Locate every malaria parasite.
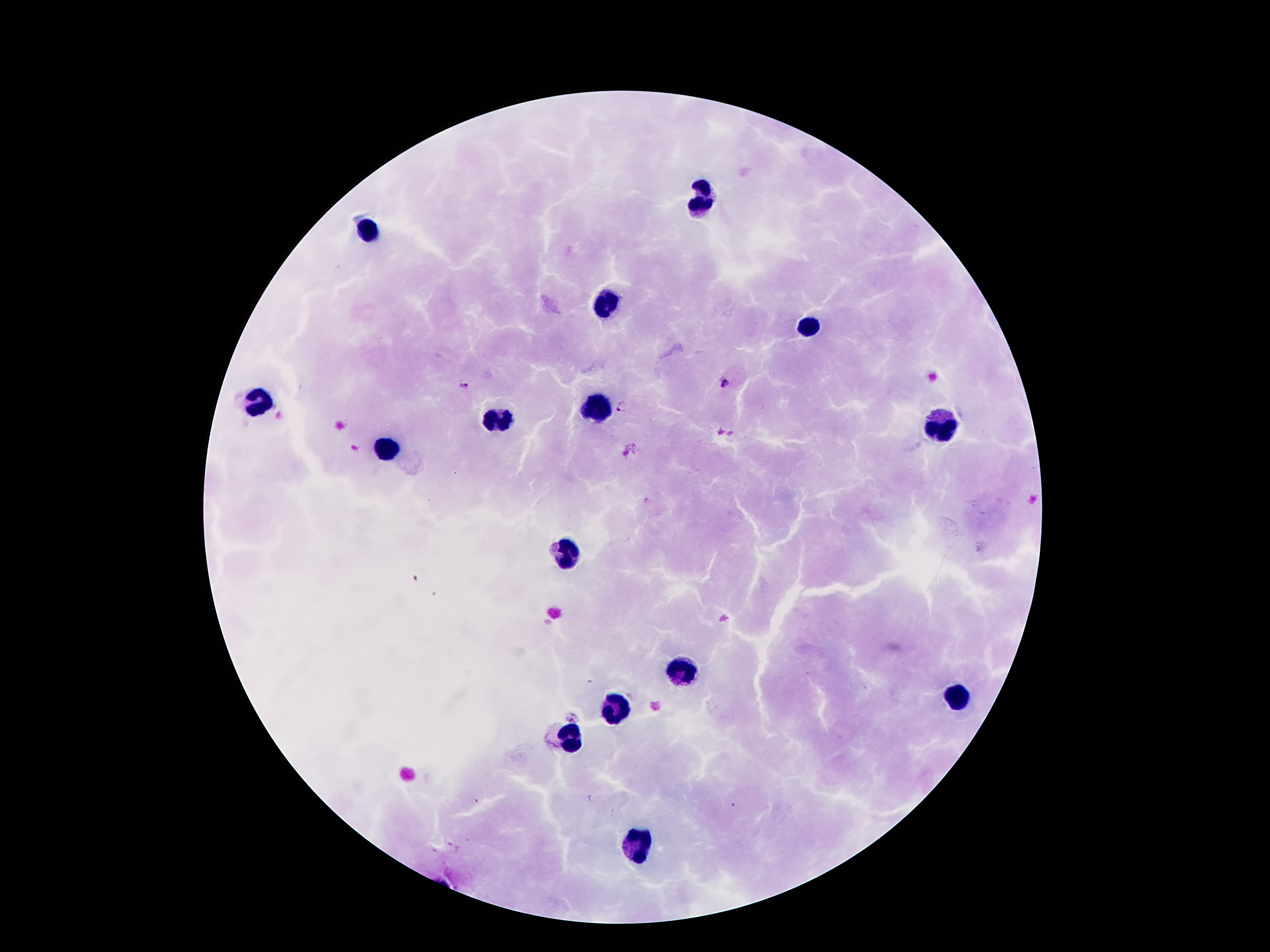

Approximate centers as (x, y) in pixels.
Malaria parasites: (464, 384), (725, 384), (622, 406).

Summary:
  - Leukocyte locations: (703, 195), (369, 231), (608, 300), (808, 324), (256, 403), (599, 406), (498, 419), (942, 425), (384, 451), (562, 548), (686, 672), (958, 694), (614, 707), (567, 740), (633, 844)
  - Field of view: one from this slide
  - Magnification: 100x
  - Stain: Giemsa
  - Preparation: thick blood film
  - Image size: 1270×952 pixels
  - Capture: smartphone camera through the microscope eyepiece
  - Patient malaria status: infected with Plasmodium falciparum